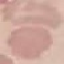

Result: negative for malaria parasites. Cell patch, automatically extracted from a larger field of view and resized to 64 × 64 pixels. Acquired by smartphone through the microscope eyepiece. Thin blood smear. Giemsa-stained preparation.